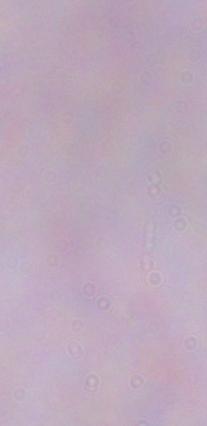

modality = micrograph
identification = trypanosome
magnification = 1000x